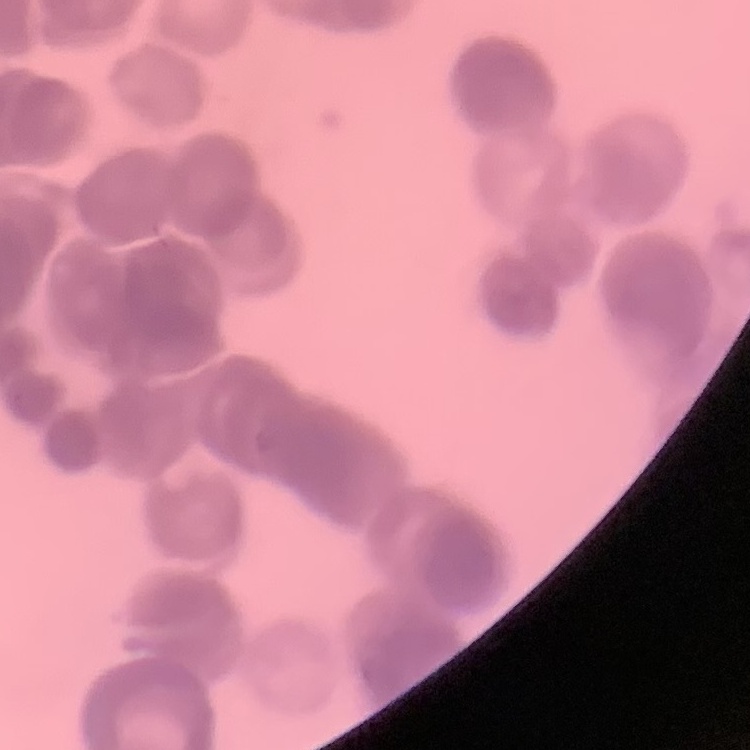
Summary:
  - Erythrocyte morphology: rouleaux formation
  - Preparation: thin blood smear
  - Stain: Field's or Giemsa
  - Image type: one tile cut from a larger photomicrograph